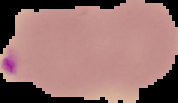 The area outside the segmented cell region is set to black. Result: malaria parasites identified. Image is 178×103 pixels. From a thin blood smear.